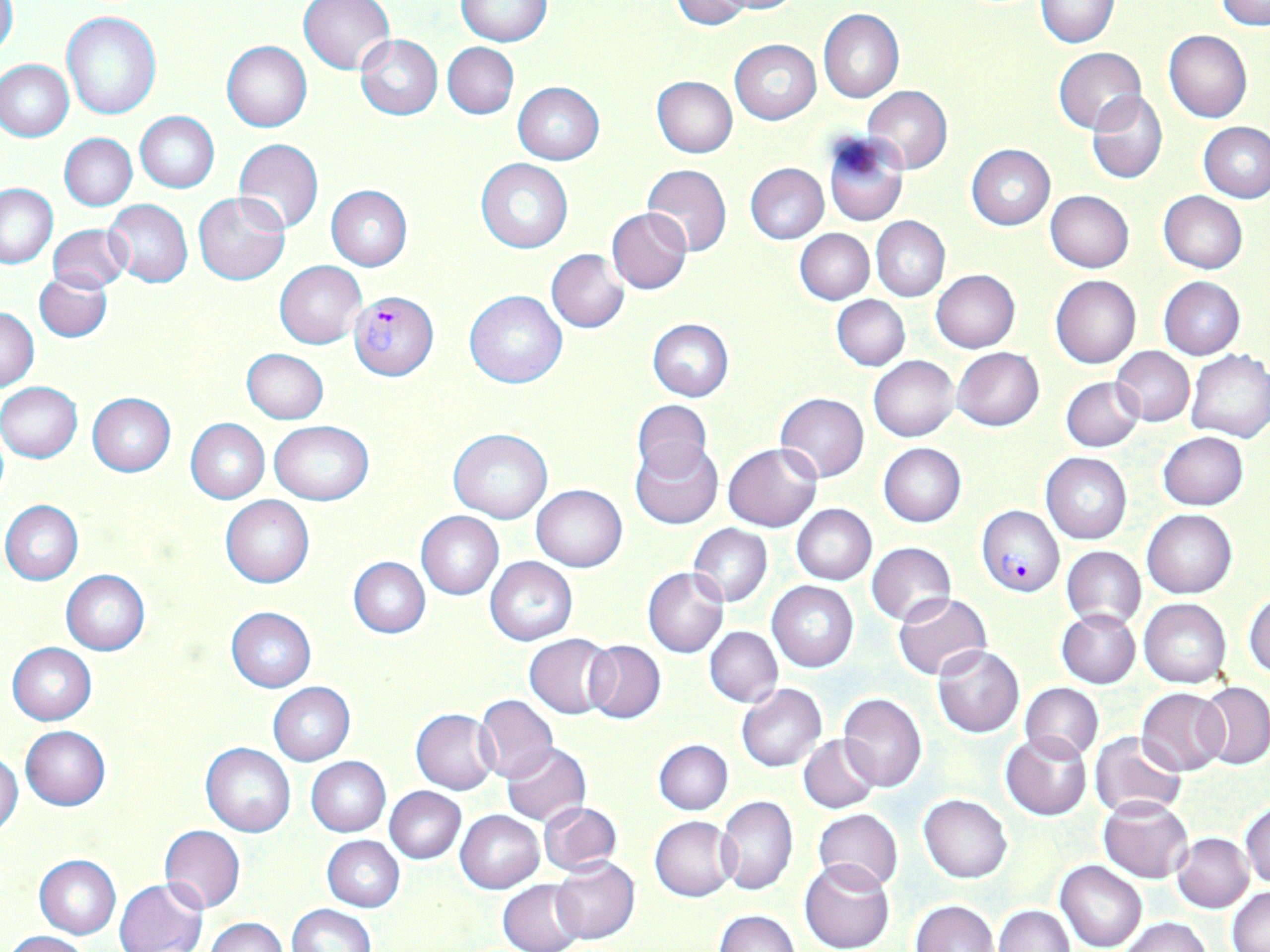 Approximate bounding boxes as (x1,y1)-(x2,y2) corner pairs in pixels. Plasmodium falciparum-infected red blood cell locations: (349,292)-(439,381), (978,506)-(1064,597). Uninfected red blood cell locations: (297,0)-(395,75), (670,0)-(752,30), (716,0)-(807,14), (1035,0)-(1118,48), (456,1)-(551,47), (1217,1)-(1270,29), (0,2)-(18,59), (818,9)-(904,102), (62,11)-(161,120), (1164,30)-(1252,122), (356,35)-(442,121), (730,40)-(821,124), (222,41)-(311,132), (443,42)-(519,119), (1053,47)-(1147,135), (1,59)-(73,141), (651,76)-(737,158), (514,82)-(604,165), (863,86)-(952,173), (1085,90)-(1168,185), (136,112)-(219,193), (1199,122)-(1270,202), (60,133)-(137,210), (823,134)-(908,227), (233,139)-(323,234), (966,144)-(1055,230), (477,158)-(573,254), (745,163)-(828,244), (642,164)-(731,258), (0,184)-(57,268), (327,185)-(411,270), (1045,190)-(1134,273), (194,192)-(289,285), (1158,192)-(1248,274), (104,199)-(193,287), (606,208)-(692,294), (872,216)-(950,302), (48,224)-(131,292), (795,228)-(874,304), (546,249)-(629,332), (275,260)-(366,349), (930,270)-(1020,353), (35,272)-(112,342), (1050,275)-(1141,369), (1159,277)-(1245,360), (465,290)-(567,388), (832,294)-(910,370), (1,307)-(39,393), (647,319)-(733,400), (1111,346)-(1195,426), (242,348)-(328,423), (953,348)-(1044,431), (1185,349)-(1270,443), (869,355)-(958,441), (1060,376)-(1144,452), (0,382)-(84,463), (88,393)-(175,476), (775,393)-(868,482), (632,400)-(712,483), (186,418)-(270,503), (270,422)-(373,505), (449,428)-(552,523), (1157,432)-(1248,510), (630,442)-(722,530), (879,443)-(966,527), (723,444)-(821,531), (1041,453)-(1131,543), (532,485)-(626,571), (221,495)-(314,588), (1,500)-(83,585), (792,504)-(876,584), (1142,509)-(1237,598), (417,511)-(503,599), (688,523)-(772,608), (866,543)-(956,626), (1061,547)-(1146,629), (349,557)-(430,638), (484,557)-(577,645), (642,567)-(729,658), (61,569)-(150,654), (768,581)-(858,671), (1245,589)-(1270,680), (894,593)-(992,680), (1139,597)-(1232,688), (226,607)-(316,692), (1057,609)-(1140,688), (704,626)-(782,708), (524,634)-(617,718), (583,639)-(665,724), (7,642)-(96,724), (932,644)-(1025,737), (267,682)-(355,765), (1020,682)-(1103,763), (1198,683)-(1270,770), (737,684)-(827,772), (1137,688)-(1229,775), (839,694)-(928,792), (475,695)-(559,781), (411,710)-(499,793), (21,726)-(111,811), (1001,732)-(1092,820), (1090,732)-(1186,819), (799,734)-(880,814), (654,739)-(732,814), (201,742)-(295,836), (501,743)-(590,825), (0,752)-(23,837), (306,756)-(390,837), (385,787)-(465,863), (919,794)-(1013,882), (717,797)-(798,895), (1099,797)-(1194,883), (537,801)-(623,874), (1242,804)-(1270,892), (813,809)-(904,893), (455,810)-(544,893), (651,816)-(738,901), (159,824)-(246,913), (1172,832)-(1254,913), (323,835)-(404,912), (34,855)-(120,939), (550,856)-(639,944), (800,859)-(895,952), (1055,860)-(1147,952), (116,878)-(208,952), (498,879)-(586,952), (1227,886)-(1270,950), (911,900)-(997,952), (286,904)-(375,952), (994,904)-(1075,952), (716,911)-(800,952), (207,918)-(288,952), (1119,918)-(1213,952), (5,931)-(90,951). Slide-level diagnosis: Plasmodium falciparum. Thin blood smear. Captured at 1000x magnification. May-Grünwald-Giemsa stain. Image is 1270×952 pixels. Single field of view. Light microscopy.